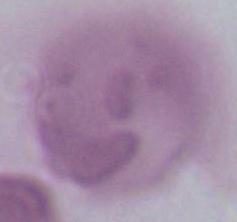 Captured at 1000x magnification. Micrograph. A red blood cell is seen.